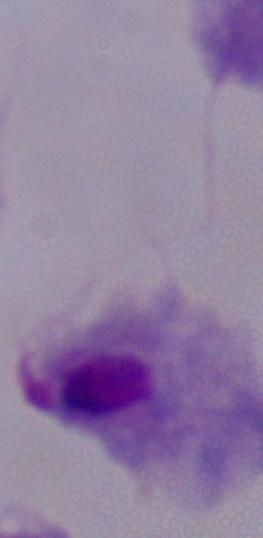 Captured at 1000x magnification. A trichomonad is shown. Micrograph.